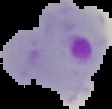
Summary:
  - Image size: 112×109 pixels
  - Preparation: thin blood film
  - Malaria status: parasitized
  - Image type: segmented cell region with the area outside set to black